Assess this cell for malaria.
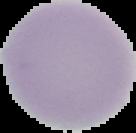
It is uninfected.

Image is 136×133 pixels. Cell region segmented out of the field of view; the surrounding area is masked to black. From a thin blood smear.